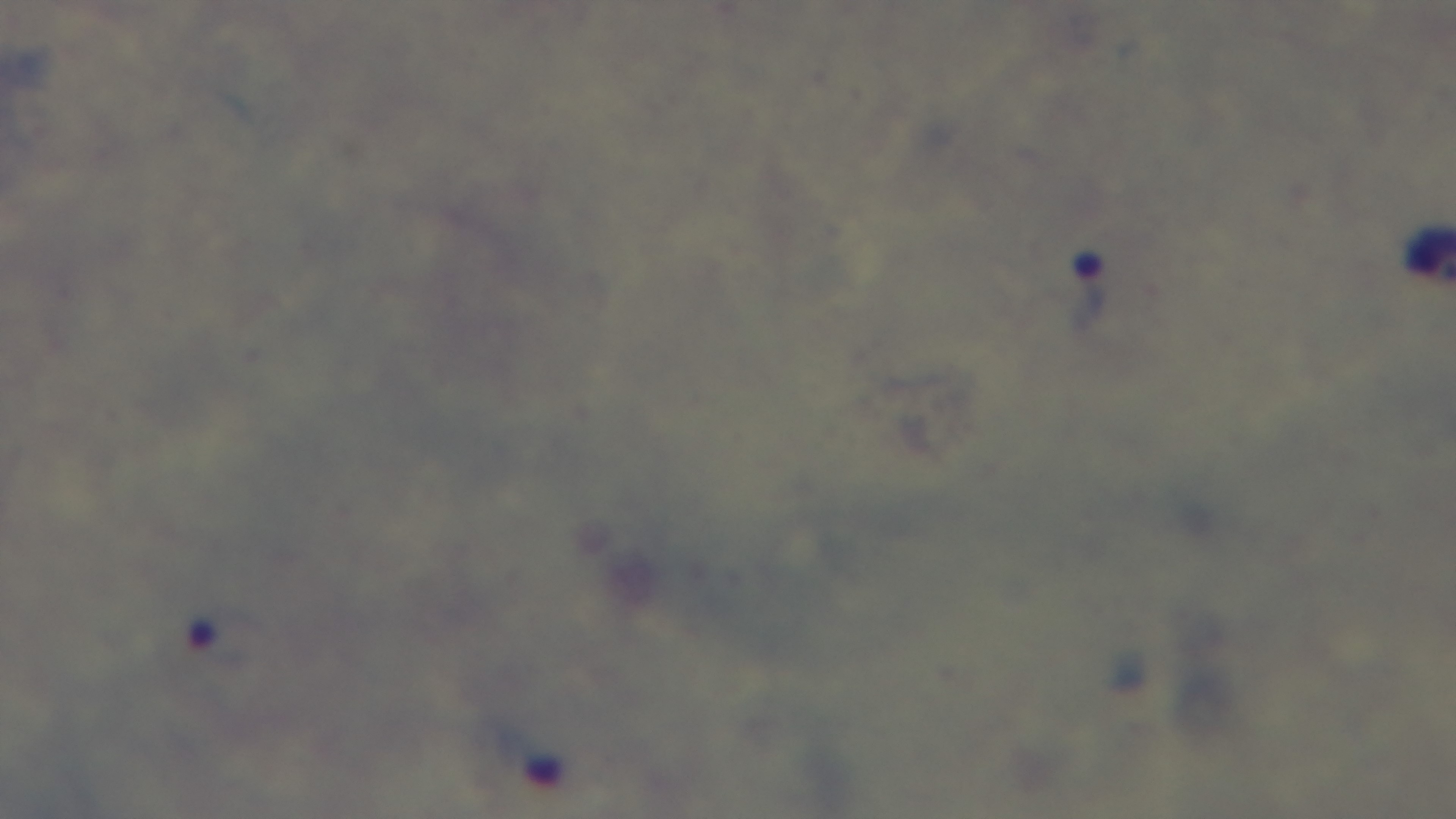

objective = 100x oil immersion
malaria status = infected
field of view = one from the slide
modality = light microscopy
stain = Giemsa
capture = mounted 4K digital camera
preparation = thick smear